Outline each Plasmodium ovale-infected red blood cell.
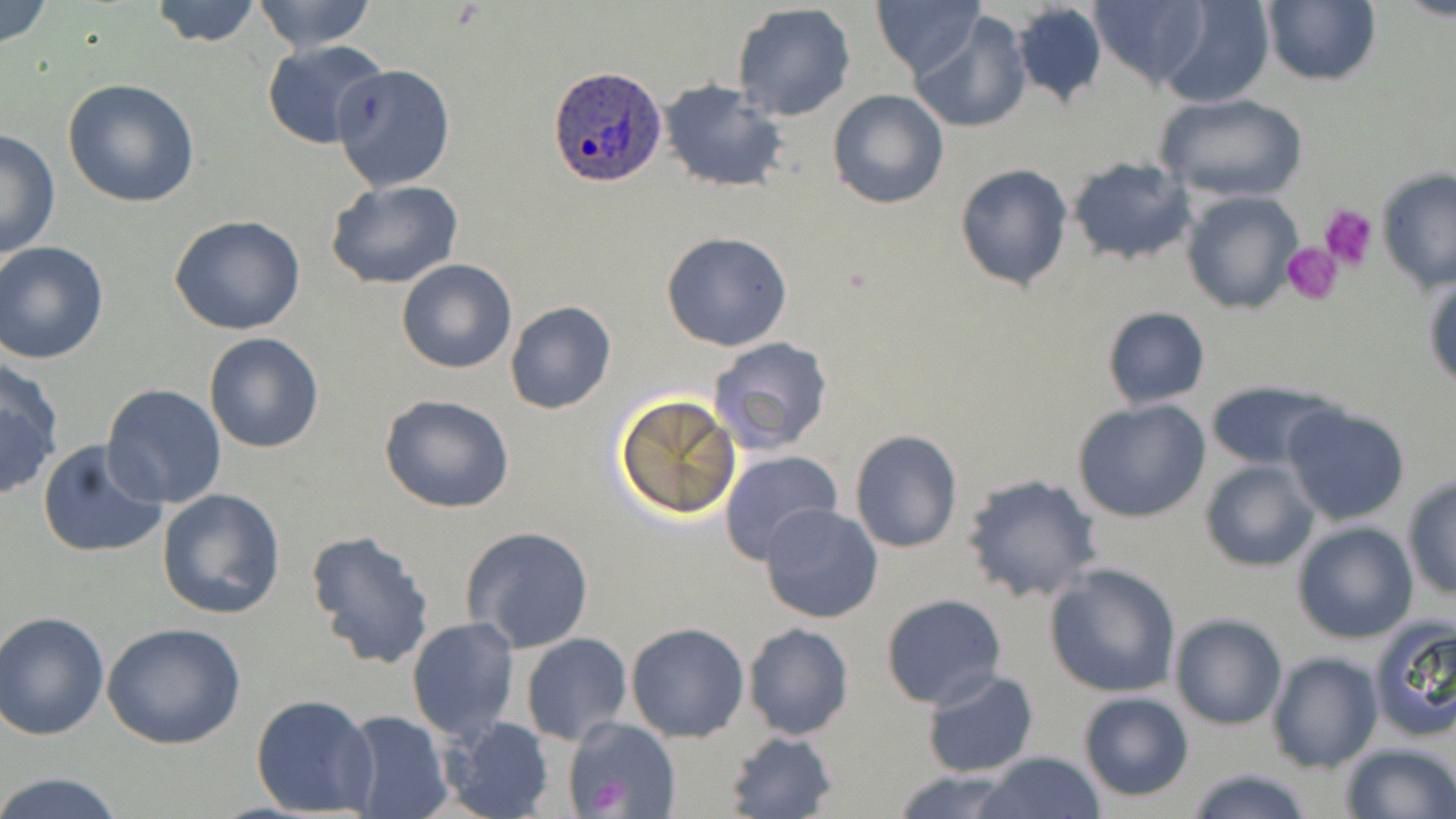
Approximate bounding boxes as (x1,y1)-(x2,y2) corner pairs in pixels.
Plasmodium ovale-infected red blood cells: (549,66)-(666,186).

Uninfected red blood cell locations: (0,0)-(53,50), (145,0)-(263,48), (248,0)-(381,53), (871,0)-(985,77), (1157,0)-(1274,108), (1090,1)-(1209,88), (1262,1)-(1381,86), (1011,2)-(1108,108), (733,3)-(855,120), (912,13)-(1032,135), (260,39)-(392,151), (332,64)-(455,191), (63,79)-(202,208), (658,80)-(788,195), (827,90)-(948,208), (1155,93)-(1306,204), (0,128)-(61,262), (1067,156)-(1196,266), (954,163)-(1074,290), (1377,167)-(1456,297), (325,179)-(463,290), (1179,189)-(1303,314), (169,215)-(308,335), (661,231)-(794,352), (0,241)-(109,364), (397,258)-(517,374), (1423,272)-(1456,389), (504,302)-(617,414), (1100,306)-(1212,409), (203,332)-(324,454), (708,336)-(834,454), (0,358)-(64,502), (1203,378)-(1339,473), (101,384)-(227,508), (613,393)-(743,522), (379,394)-(515,513), (1071,398)-(1210,522), (1280,403)-(1411,527), (849,429)-(963,554), (36,439)-(168,557), (1236,445)-(1388,568), (719,450)-(845,568), (1198,459)-(1321,572), (962,473)-(1103,603), (1402,476)-(1456,600), (156,488)-(286,620), (759,502)-(885,624), (1291,521)-(1418,643), (461,526)-(594,652), (306,528)-(436,672), (1044,562)-(1181,699), (880,593)-(1007,709), (2,610)-(111,740), (1169,613)-(1287,730), (406,617)-(520,740), (1368,618)-(1456,743), (625,622)-(749,741), (742,622)-(854,740), (101,623)-(246,751), (521,633)-(635,745), (1267,653)-(1381,772), (922,669)-(1039,779), (1078,690)-(1195,802), (249,693)-(379,817), (340,711)-(453,819), (442,716)-(554,819), (563,718)-(680,819), (723,730)-(838,818), (1340,742)-(1456,819), (977,750)-(1107,819), (1185,766)-(1314,819), (893,770)-(1024,818), (0,771)-(128,819). Platelet locations: (1321,203)-(1377,273), (1282,240)-(1344,305). Slide-level diagnosis: Plasmodium ovale. Single field of view. Optical microscopy. 1000x magnification. May-Grünwald-Giemsa-stained preparation. Image is 1456×819 pixels. Thin blood smear.